Report the malaria status of this cell.
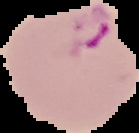
Parasitized.

preparation = thin blood smear
image type = cell region segmented out of the field of view; surrounding area masked to black
image size = 139×133 pixels